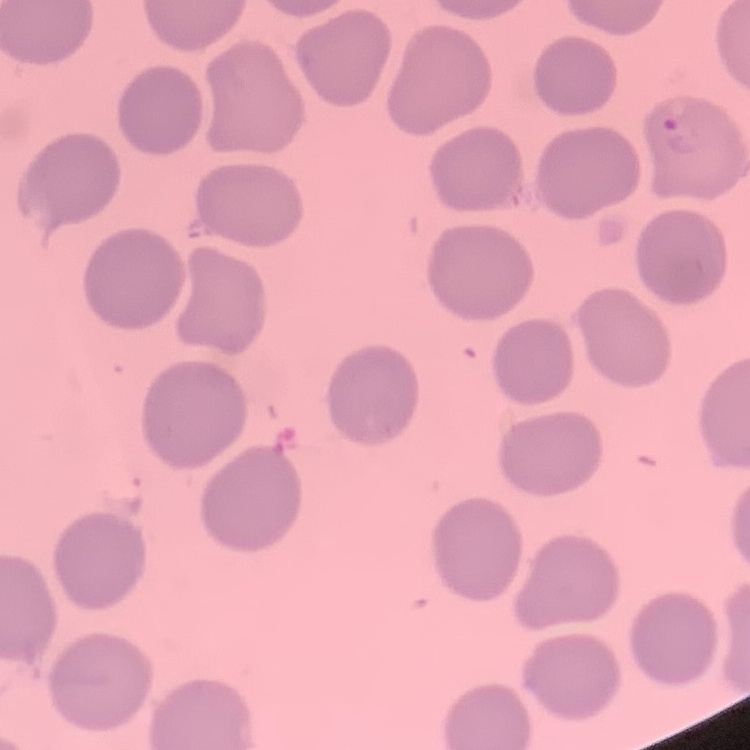
Summary:
  - Erythrocyte morphology: no rouleaux formation
  - Image type: square crop of a larger photomicrograph
  - Stain: Field's or Giemsa
  - Preparation: thin blood film